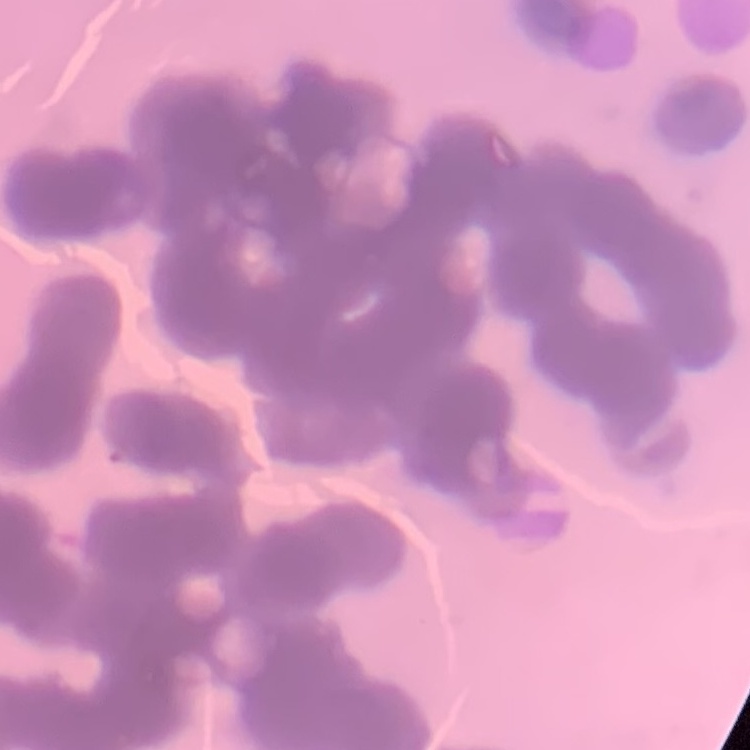
Summary:
  - Erythrocyte morphology: rouleaux formation
  - Stain: Field's or Giemsa
  - Preparation: thin peripheral smear
  - Image type: one tile cut from a larger photomicrograph